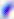

Summary:
  - Modality: micrograph
  - Identification: Toxoplasma gondii
  - Magnification: 400x